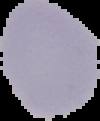
image type = cell region segmented out of the field of view; surrounding area masked to black
result = no malaria parasites seen
image size = 100×121 pixels
preparation = thin blood film